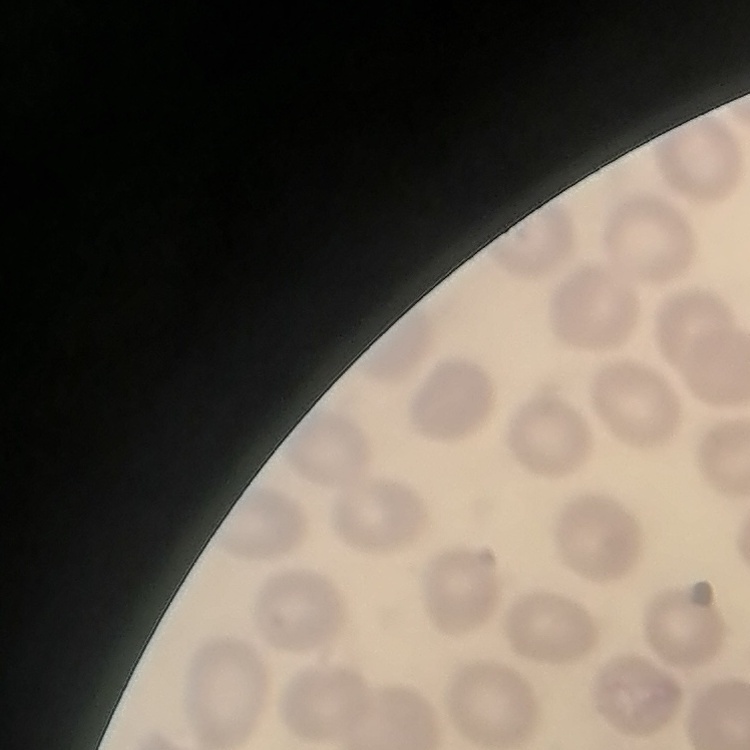

Summary:
  - Red blood cell morphology: no rouleaux formation
  - Image type: one tile cut from a larger photomicrograph
  - Stain: Field's or Giemsa
  - Preparation: thin blood film